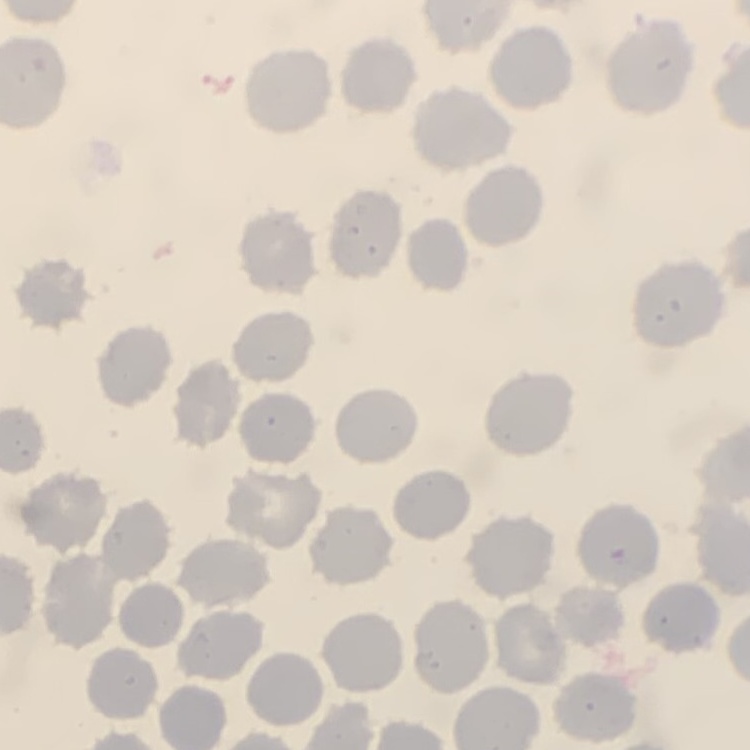

Summary:
  - Red blood cell morphology: no rouleaux formation
  - Preparation: thin blood smear
  - Image type: square crop of a larger photomicrograph
  - Stain: Field's or Giemsa